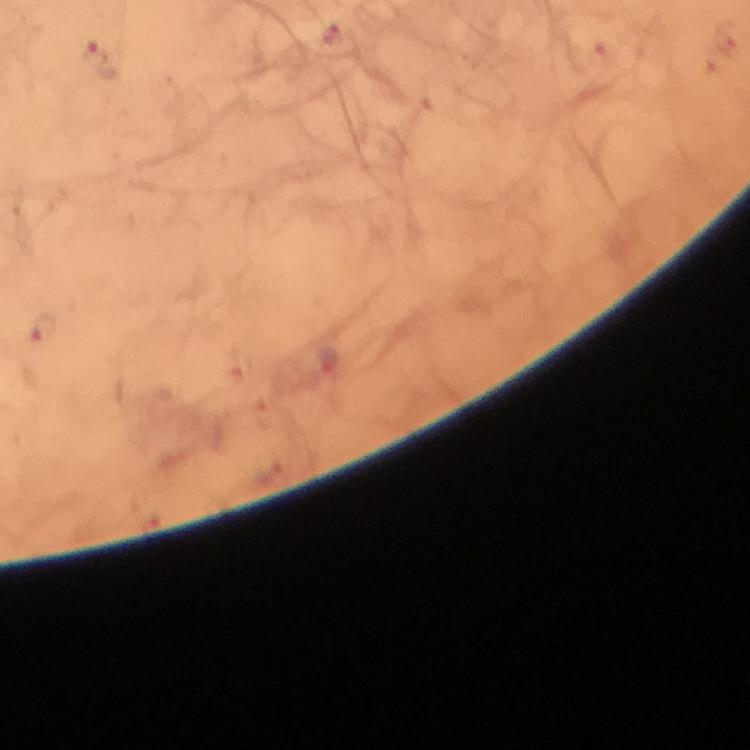

Approximate centers as (x, y) in pixels. Plasmodium parasite locations: (97, 56), (39, 329). Cropped region of a single field of view. 100x magnification. Thick blood smear. Image is 750×750 pixels. From a diagnostic examination for malaria. Giemsa-stained preparation. Immersion oil was used. Photographed through the microscope with a smartphone camera.